Classify this cell by malaria status.
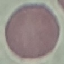
It is uninfected.

Summary:
  - Image type: cell patch, automatically extracted from a larger field of view and resized to 64 × 64 pixels
  - Preparation: thin smear
  - Capture: smartphone through the microscope eyepiece
  - Stain: Giemsa